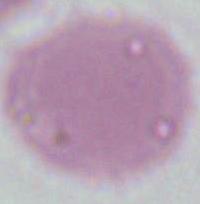
Summary:
  - Modality: micrograph
  - Identification: red blood cell
  - Magnification: 1000x